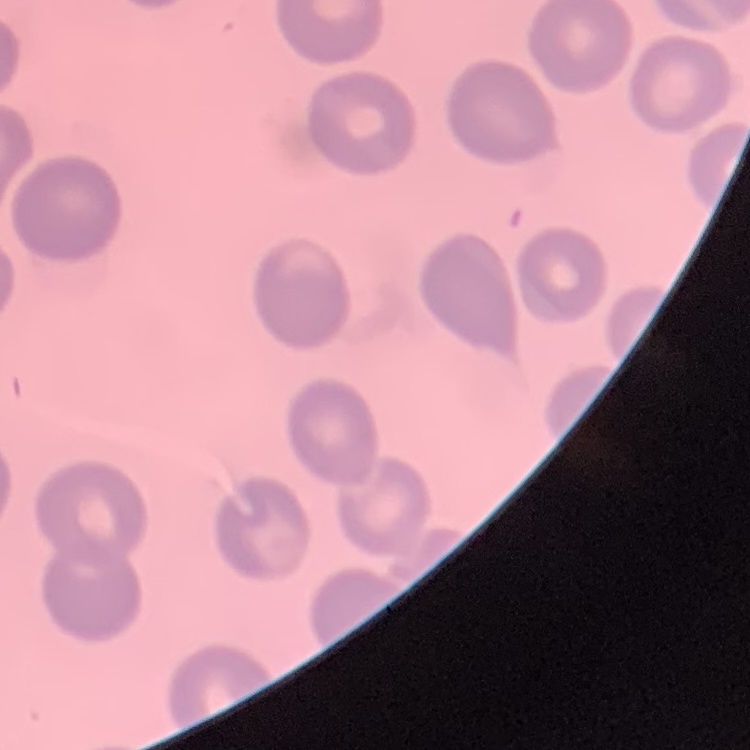

erythrocyte morphology = no rouleaux formation
preparation = thin blood smear
image type = one tile cut from a larger photomicrograph
stain = Field's or Giemsa